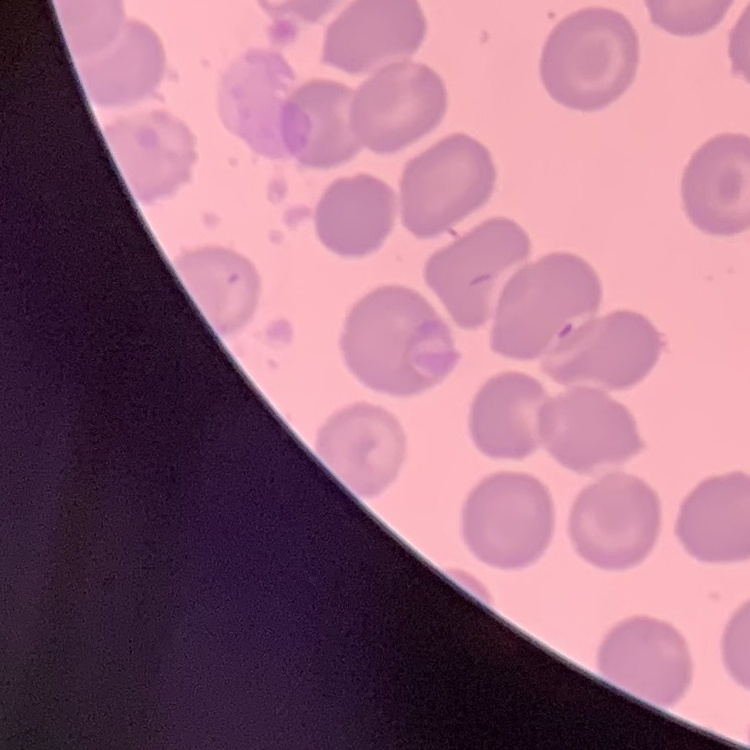
Summary:
  - Erythrocyte morphology: no rouleaux formation
  - Stain: Field's or Giemsa
  - Preparation: thin blood smear
  - Image type: square crop of a larger photomicrograph